Classify this cell by malaria status.
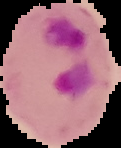
It is parasitized.

Summary:
  - Preparation: thin blood smear
  - Image type: cell region segmented out of the field of view; surrounding area masked to black
  - Image size: 121×148 pixels